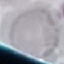

Summary:
  - Result: negative for malaria parasites
  - Preparation: thin blood film
  - Stain: Giemsa
  - Capture: smartphone camera at the microscope eyepiece
  - Image type: cell patch, automatically extracted from a larger field of view and resized to 64 × 64 pixels